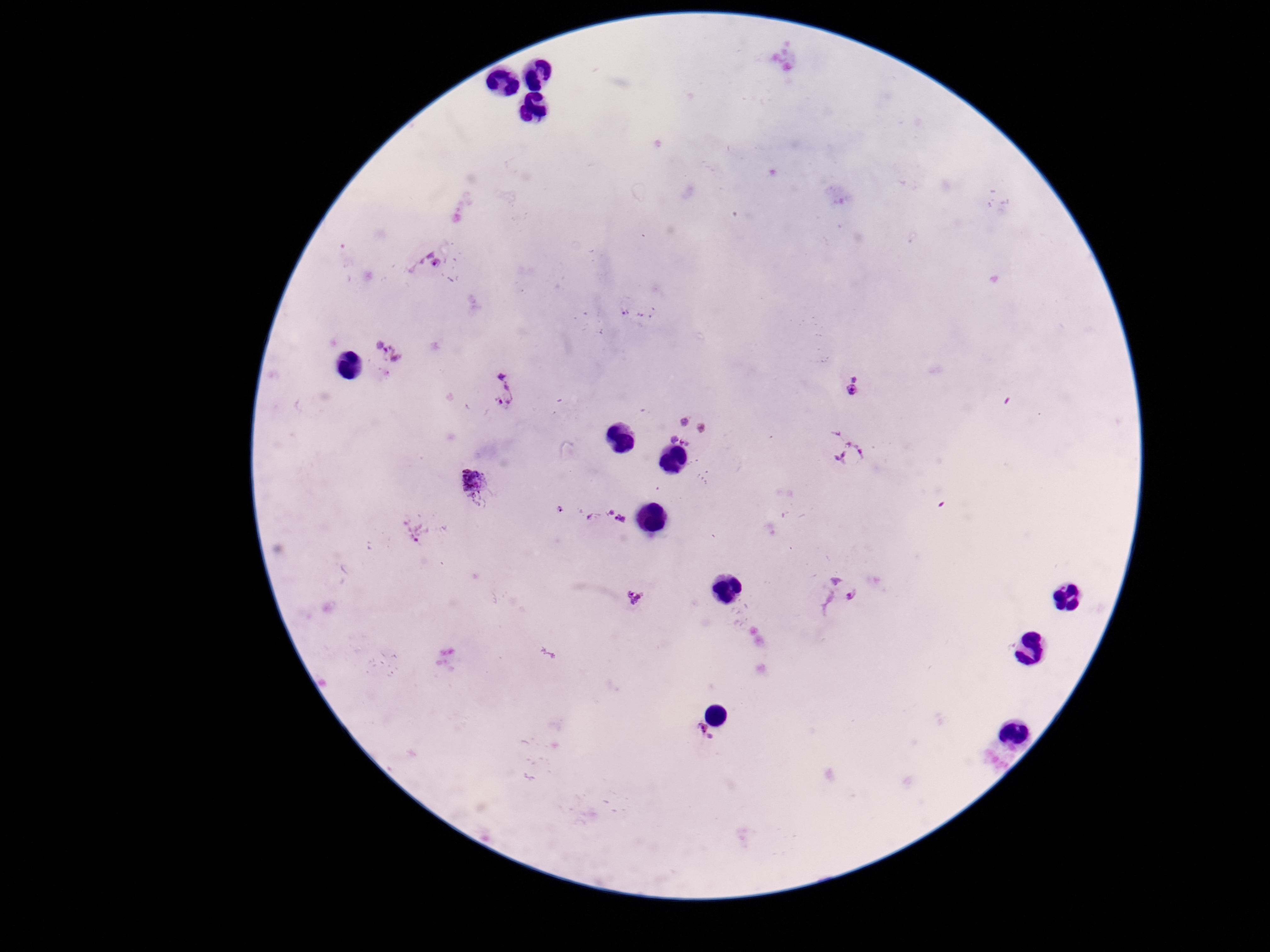
{
  "magnification": "100x",
  "capture": "smartphone camera through the microscope eyepiece",
  "image_size": "1270×952 pixels",
  "field_of_view": "single",
  "plasmodium_parasite_locations": "approximate centers as {x, y} in pixels: {429, 262}, {388, 355}, {855, 388}, {504, 390}, {688, 430}, {844, 451}, {472, 477}, {603, 519}, {417, 530}, {837, 593}, {635, 600}, {702, 734}",
  "preparation": "thick peripheral-blood smear",
  "patient_malaria_status": "positive",
  "stain": "Giemsa"
}